Identify the parasite.
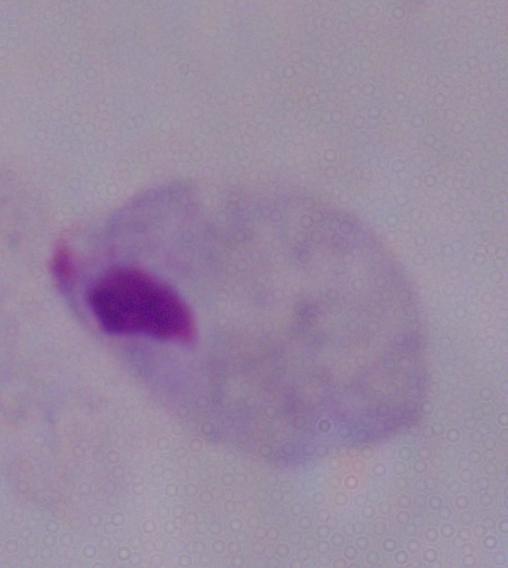

This is a trichomonad.

Photomicrograph. Captured at 1000x magnification.